Classify this cell by malaria status.
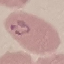

It is parasitized.

Summary:
  - Image type: cell patch, automatically extracted from a larger field of view and resized to 64 × 64 pixels
  - Preparation: thin smear
  - Capture: smartphone camera at the microscope eyepiece
  - Stain: Giemsa